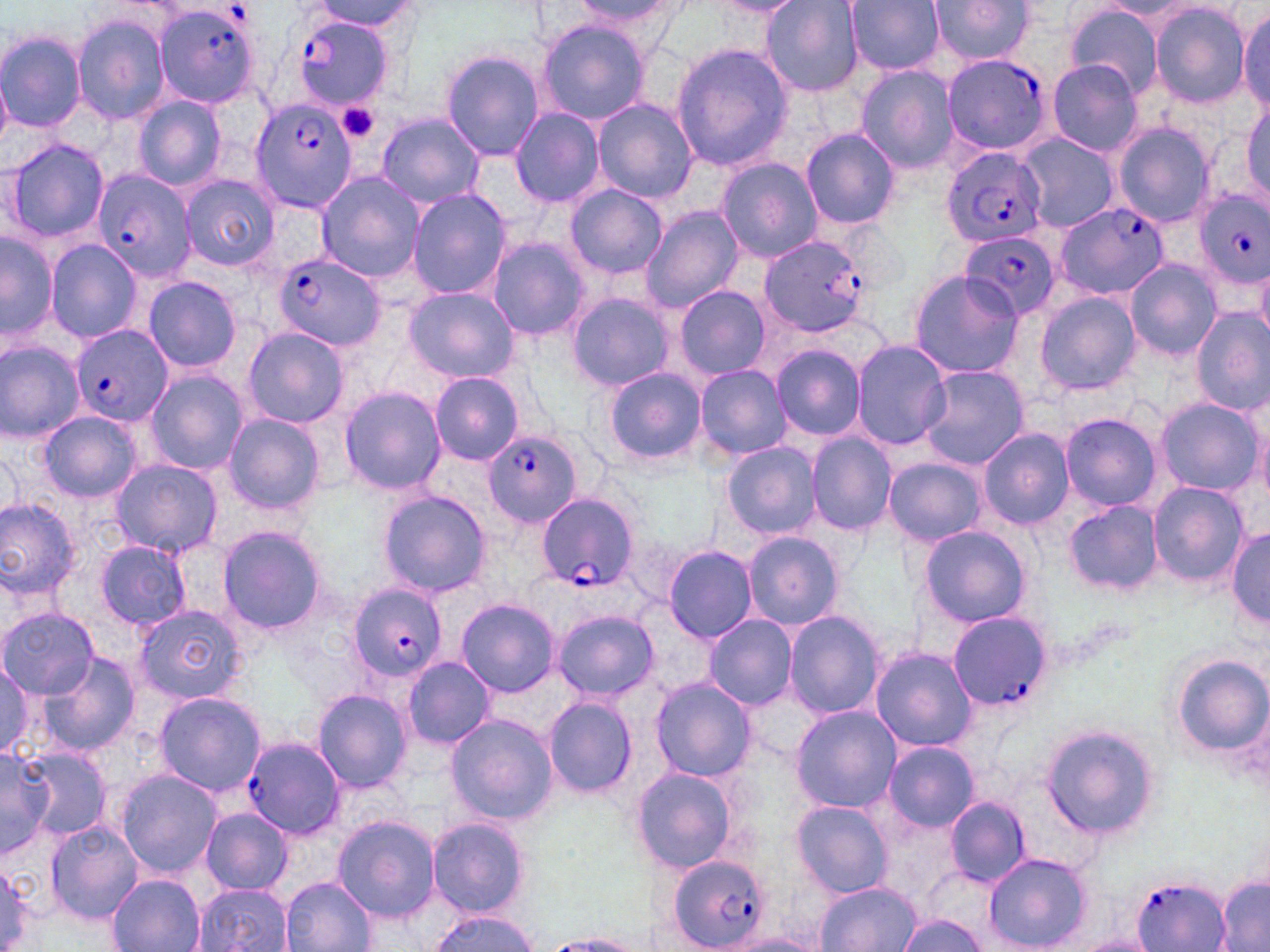 Approximate bounding boxes as [x1, y1, x2, y2] in pixels. Uninfected red blood cell locations: [312, 0, 419, 35], [573, 0, 684, 40], [761, 0, 863, 98], [845, 0, 946, 74], [927, 0, 1037, 67], [712, 1, 804, 16], [1103, 1, 1200, 22], [1149, 1, 1253, 109], [1065, 3, 1165, 96], [1236, 5, 1269, 119], [72, 13, 172, 126], [536, 19, 651, 127], [0, 29, 87, 134], [671, 41, 795, 173], [441, 50, 544, 161], [1047, 59, 1144, 156], [856, 62, 960, 173], [131, 94, 228, 193], [1242, 95, 1270, 202], [594, 98, 697, 202], [509, 109, 605, 208], [377, 114, 484, 209], [1112, 122, 1215, 228], [801, 128, 899, 230], [1016, 132, 1119, 233], [5, 139, 109, 249], [717, 158, 824, 262], [314, 170, 424, 282], [180, 175, 279, 271], [565, 183, 667, 278], [407, 189, 512, 300], [640, 206, 744, 314], [1, 231, 56, 346], [487, 238, 590, 340], [45, 239, 143, 342], [1124, 257, 1221, 361], [1254, 260, 1270, 340], [909, 269, 1022, 378], [142, 277, 243, 372], [673, 285, 770, 381], [403, 287, 518, 384], [566, 292, 675, 391], [1036, 292, 1139, 394], [1191, 310, 1269, 413], [241, 327, 349, 428], [0, 338, 87, 444], [852, 340, 951, 450], [771, 345, 866, 440], [918, 364, 1029, 469], [695, 365, 792, 461], [603, 366, 707, 467], [145, 370, 248, 473], [430, 373, 525, 465], [339, 387, 446, 495], [1154, 396, 1262, 496], [40, 410, 142, 502], [221, 412, 326, 517], [1060, 412, 1162, 512], [1253, 419, 1270, 508], [978, 428, 1073, 529], [807, 433, 895, 536], [723, 443, 822, 540], [108, 458, 222, 557], [883, 458, 987, 545], [1149, 483, 1247, 584], [379, 491, 490, 598], [0, 498, 84, 602], [1066, 502, 1162, 594], [217, 525, 329, 636], [921, 527, 1029, 628], [1229, 529, 1270, 629], [742, 531, 845, 630], [95, 540, 192, 631], [662, 545, 759, 643], [457, 598, 559, 697], [132, 602, 249, 706], [1, 608, 98, 698], [551, 609, 658, 703], [784, 610, 885, 720], [704, 615, 798, 709], [868, 646, 978, 752], [1169, 654, 1270, 757], [401, 656, 496, 749], [39, 657, 141, 758], [0, 661, 45, 761], [650, 677, 756, 783], [312, 689, 414, 792], [153, 691, 267, 797], [542, 694, 638, 799], [791, 707, 900, 812], [445, 713, 557, 824], [1040, 725, 1159, 840], [884, 741, 978, 831], [23, 746, 112, 841], [0, 747, 52, 860], [633, 767, 742, 874], [113, 770, 224, 879], [943, 796, 1030, 887], [791, 800, 893, 897], [198, 808, 292, 895], [332, 816, 444, 923], [426, 817, 530, 918], [44, 821, 141, 924], [982, 852, 1092, 951], [1, 861, 40, 949], [107, 874, 205, 951], [1216, 875, 1269, 952], [281, 876, 376, 951], [813, 881, 921, 952], [192, 884, 293, 952], [427, 911, 539, 952], [895, 913, 986, 952], [545, 934, 645, 951], [1062, 934, 1158, 952]. Platelet locations: [338, 102, 381, 143]. Plasmodium falciparum-infected red blood cell locations: [157, 2, 263, 108], [289, 15, 394, 110], [943, 54, 1052, 157], [249, 99, 355, 212], [942, 146, 1046, 249], [92, 167, 196, 281], [1195, 189, 1270, 289], [1058, 203, 1166, 299], [960, 230, 1059, 323], [759, 235, 874, 337], [273, 252, 386, 350], [69, 324, 171, 428], [483, 429, 581, 527], [535, 493, 639, 590], [346, 583, 445, 683], [946, 611, 1051, 710], [241, 735, 346, 841], [667, 854, 772, 950], [1131, 876, 1233, 952]. Slide-level diagnosis: Plasmodium falciparum. Light microscopy. May-Grünwald-Giemsa-stained preparation. 1000x magnification. One field of a larger specimen. Thin blood film. Image is 1270×952 pixels.